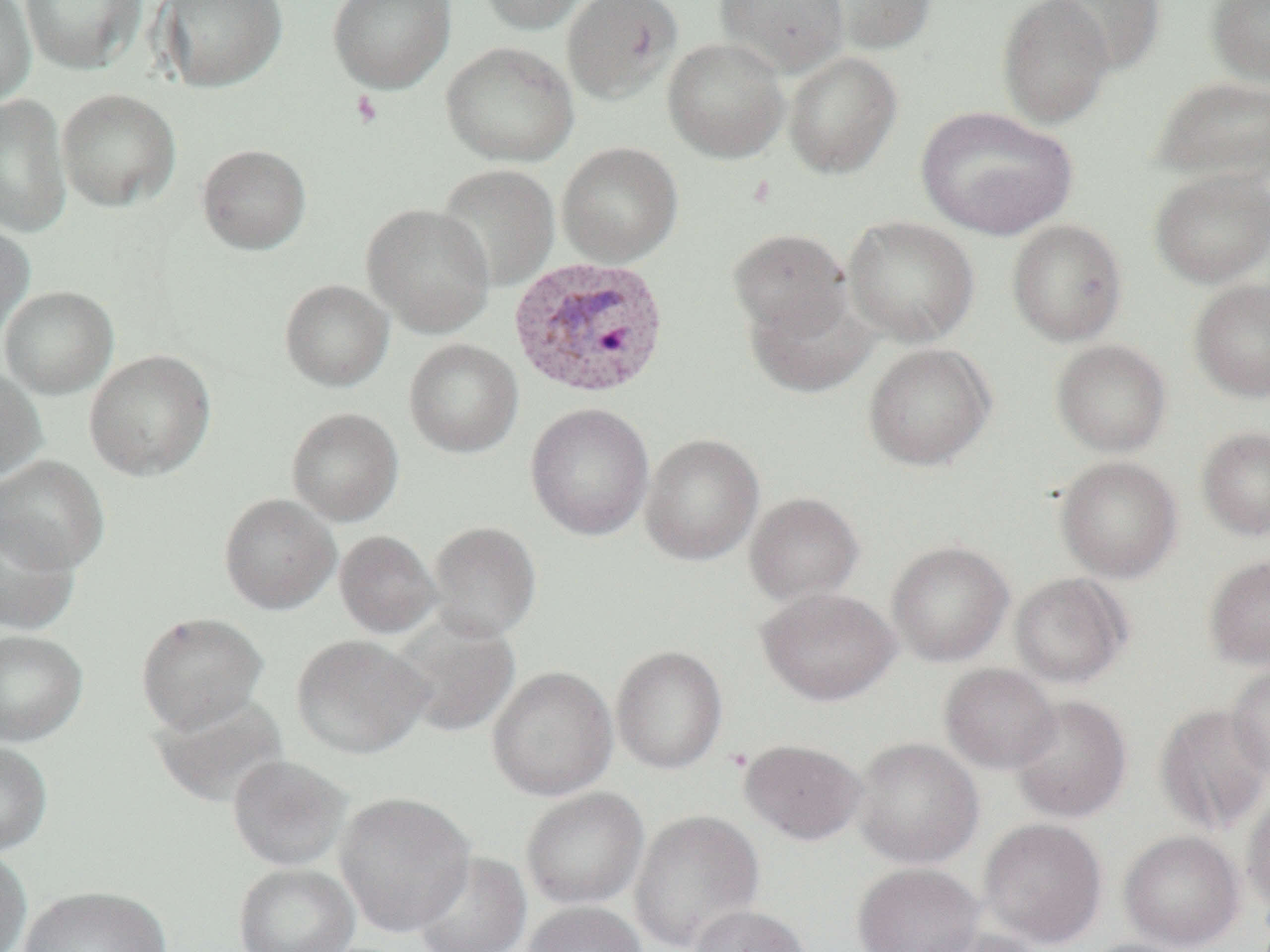
Summary:
  - Coordinate format: approximate bounding boxes as [x1, y1, x2, y2] in pixels
  - Platelet locations: [351, 90, 382, 128]
  - Uninfected red blood cell locations: [0, 0, 36, 106], [20, 0, 146, 75], [158, 0, 288, 93], [328, 0, 456, 93], [477, 0, 592, 35], [561, 0, 683, 105], [715, 0, 849, 77], [815, 0, 937, 55], [997, 0, 1115, 129], [1047, 0, 1166, 75], [1206, 0, 1270, 87], [662, 37, 790, 163], [441, 41, 579, 167], [782, 50, 903, 179], [1152, 75, 1270, 185], [56, 88, 181, 212], [0, 95, 72, 238], [916, 106, 1076, 239], [557, 142, 683, 266], [196, 144, 312, 255], [436, 164, 560, 291], [1150, 169, 1270, 288], [362, 203, 495, 338], [843, 216, 979, 347], [1006, 219, 1128, 346], [0, 220, 35, 342], [727, 228, 852, 341], [1189, 277, 1270, 402], [279, 279, 394, 391], [0, 286, 118, 399], [745, 289, 877, 399], [404, 338, 523, 458], [1050, 339, 1172, 457], [863, 343, 996, 471], [84, 349, 216, 481], [0, 367, 47, 483], [525, 403, 654, 541], [286, 408, 404, 526], [1196, 427, 1270, 541], [640, 433, 764, 566], [0, 456, 109, 573], [1055, 456, 1182, 583], [744, 492, 864, 604], [218, 493, 340, 615], [0, 511, 80, 635], [427, 520, 542, 642], [335, 530, 440, 639], [886, 541, 1014, 666], [1204, 555, 1270, 670], [1009, 572, 1131, 688], [757, 587, 901, 706], [135, 611, 268, 733], [388, 616, 520, 739], [0, 628, 88, 746], [291, 634, 431, 759], [611, 645, 728, 774], [939, 663, 1059, 774], [1226, 663, 1270, 783], [486, 666, 617, 802], [149, 692, 289, 809], [1009, 695, 1132, 822], [1154, 703, 1270, 835], [852, 737, 983, 868], [740, 738, 867, 844], [0, 741, 53, 855], [226, 754, 352, 872], [521, 787, 649, 909], [1242, 790, 1270, 914], [334, 791, 476, 937], [630, 810, 765, 950], [978, 818, 1108, 948], [1119, 830, 1244, 950], [0, 847, 32, 952], [412, 851, 532, 952], [234, 862, 360, 952], [852, 862, 983, 952], [17, 885, 172, 952], [523, 901, 648, 952], [688, 904, 812, 952], [914, 926, 1046, 952], [1077, 938, 1196, 952]
  - Plasmodium vivax-infected red blood cell locations: [508, 255, 671, 400]
  - Slide-level diagnosis: Plasmodium vivax
  - Image size: 1270×952 pixels
  - Modality: light microscopy
  - Field of view: single
  - Magnification: 1000x
  - Preparation: thin blood smear